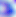

Summary:
  - Identification: Toxoplasma gondii
  - Magnification: 400x
  - Modality: micrograph